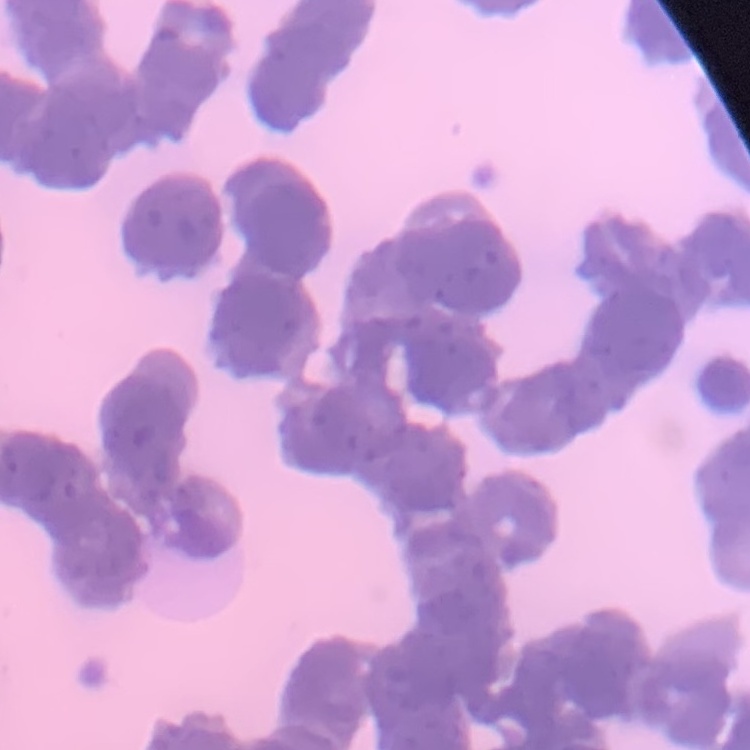

Summary:
  - Erythrocyte morphology: rouleaux formation
  - Stain: Field's or Giemsa
  - Preparation: thin blood smear
  - Image type: one tile cut from a larger photomicrograph